Report the malaria status of this cell.
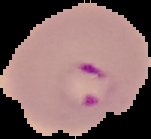

It is parasitized.

Summary:
  - Image size: 151×139 pixels
  - Preparation: thin blood smear
  - Image type: segmented cell region with the area outside set to black